Point out each Plasmodium parasite.
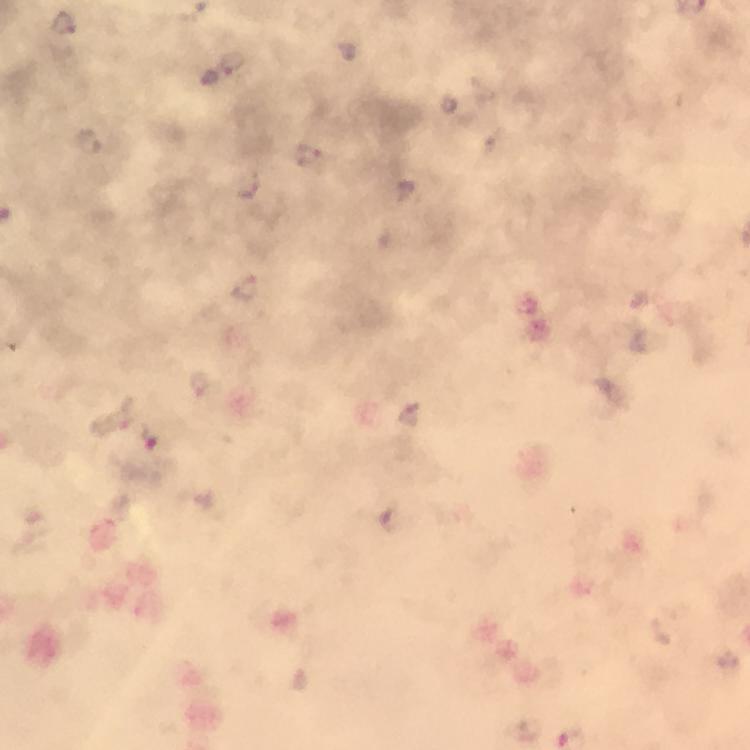
Approximate centers as {x, y} in pixels.
Plasmodium parasites: {65, 23}, {232, 63}, {85, 142}, {309, 157}, {248, 185}, {245, 290}, {114, 420}, {152, 438}.

{
  "context": "from a malaria diagnostic workup",
  "image_size": "750×750 pixels",
  "capture": "smartphone camera through the microscope",
  "immersion_oil": "used",
  "cropped_from": "one field of view",
  "preparation": "thick smear",
  "stain": "Giemsa",
  "magnification": "100x"
}